Assess this cell for malaria.
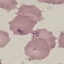

It is uninfected.

Summary:
  - Stain: Giemsa
  - Preparation: thin blood smear
  - Capture: smartphone camera at the microscope eyepiece
  - Image type: cell patch, automatically extracted from a larger field of view and resized to 64 × 64 pixels